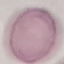
Summary:
  - Malaria status: uninfected
  - Preparation: thin smear
  - Capture: smartphone camera at the microscope eyepiece
  - Image type: automatically extracted cell patch, resized to 64 × 64 pixels
  - Stain: Giemsa